Classify this cell by malaria status.
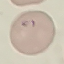
Parasitized.

stain = Giemsa
image type = cell patch, automatically extracted from a larger field of view and resized to 64 × 64 pixels
preparation = thin blood film
capture = smartphone through the microscope eyepiece